Comment on the morphology of the erythrocytes.
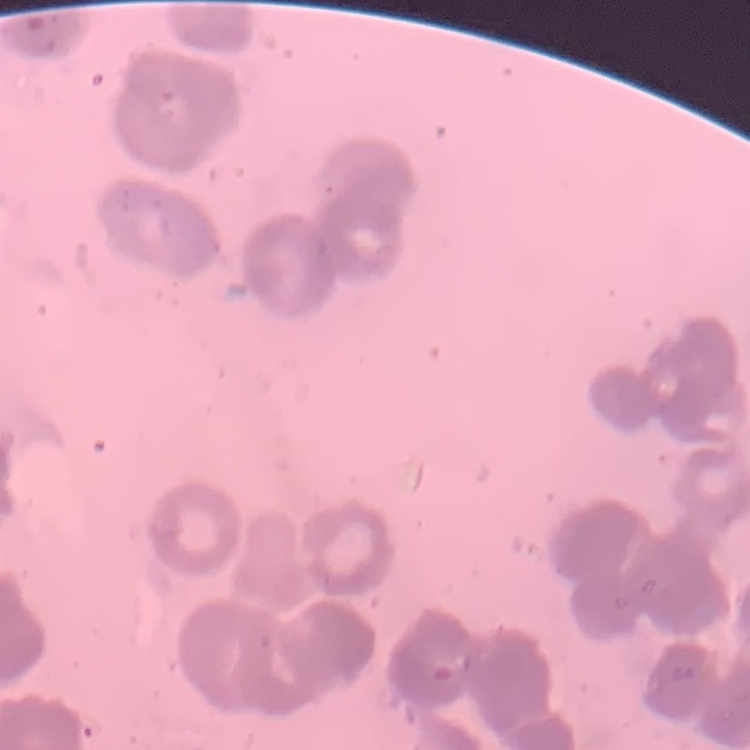

They show rouleaux formation.

Summary:
  - Image type: one tile cut from a larger photomicrograph
  - Stain: Field's or Giemsa
  - Preparation: thin blood smear